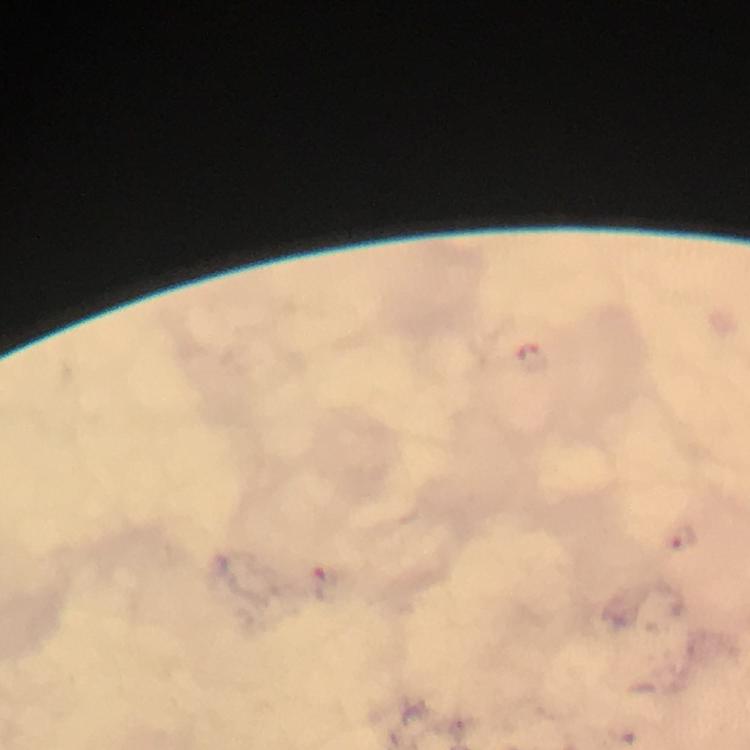

{
  "image_size": "750×750 pixels",
  "stain": "Giemsa",
  "capture": "smartphone camera through the microscope",
  "malaria_parasite_locations": "approximate centers as {x, y} in pixels: {684, 538}",
  "immersion_oil": "applied",
  "magnification": "100x",
  "cropped_from": "a single field of view",
  "context": "from a malaria diagnostic workup",
  "preparation": "thick blood smear"
}